Locate Plasmodium falciparum parasites and identify their life-cycle stages.
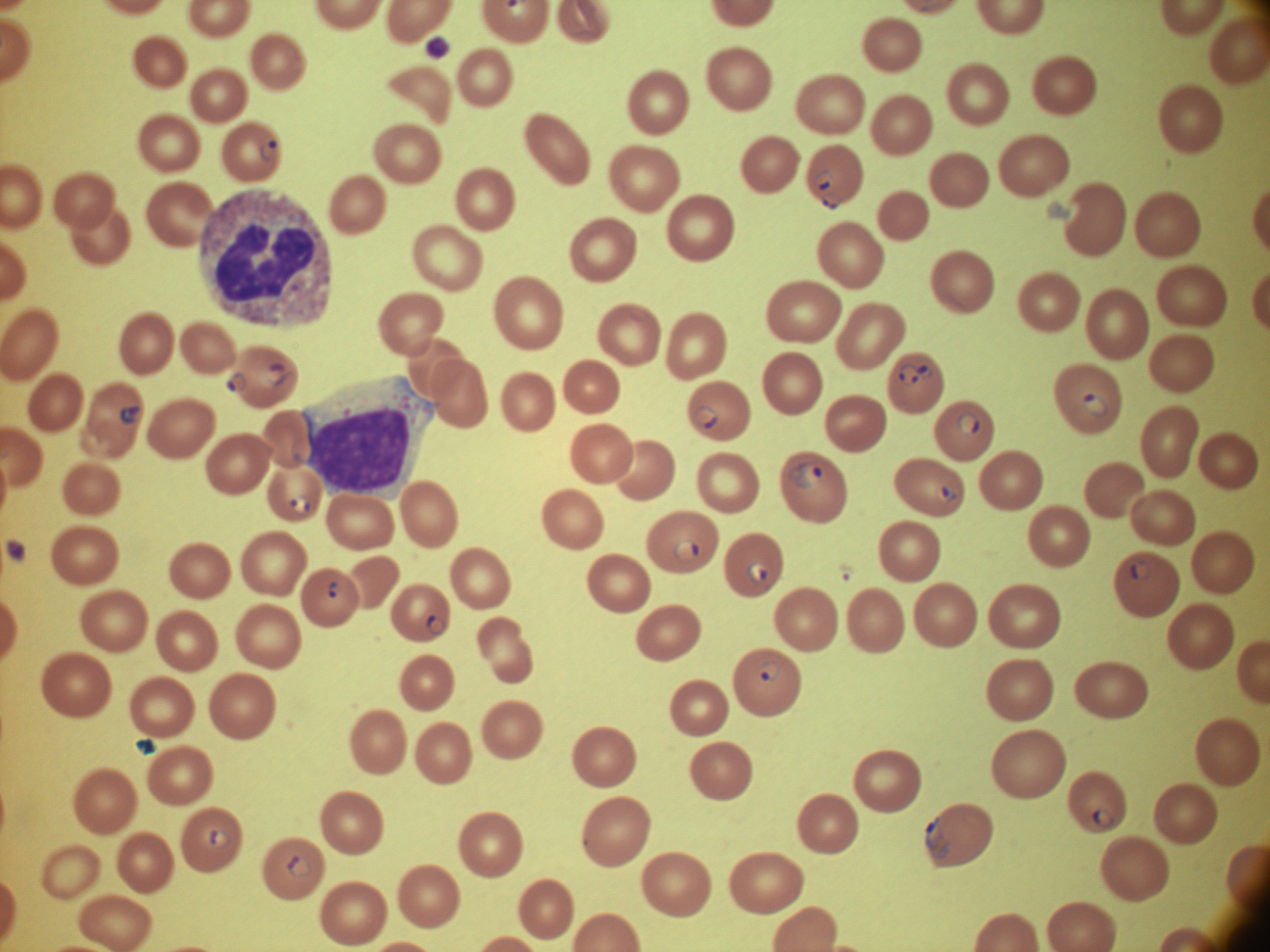
Approximate bounding boxes as [x1, y1, x2, y2] in pixels, from the source annotation, which is not necessarily exhaustive.
Ring forms: [260, 139, 278, 162], [812, 169, 834, 190], [822, 193, 840, 210], [265, 362, 286, 387], [898, 362, 920, 387], [920, 364, 933, 381], [225, 371, 247, 394], [1082, 392, 1109, 417], [119, 404, 141, 425], [692, 405, 717, 429], [957, 411, 980, 436], [789, 463, 822, 490], [937, 484, 957, 503], [289, 494, 311, 514], [673, 539, 699, 563], [747, 560, 768, 582], [1131, 560, 1152, 582], [327, 581, 339, 598], [425, 615, 447, 636], [759, 661, 780, 682], [1092, 809, 1114, 829], [925, 816, 951, 858], [208, 828, 232, 849], [287, 855, 310, 877].

Summary:
  - Field of view: one from this slide
  - Stain: Giemsa
  - Species: Plasmodium falciparum
  - Image size: 1270×952 pixels
  - Magnification: 100x
  - Microscope: Leica DM2000 with built-in camera
  - Preparation: thin blood smear